Outline each blood parasite and name the species.
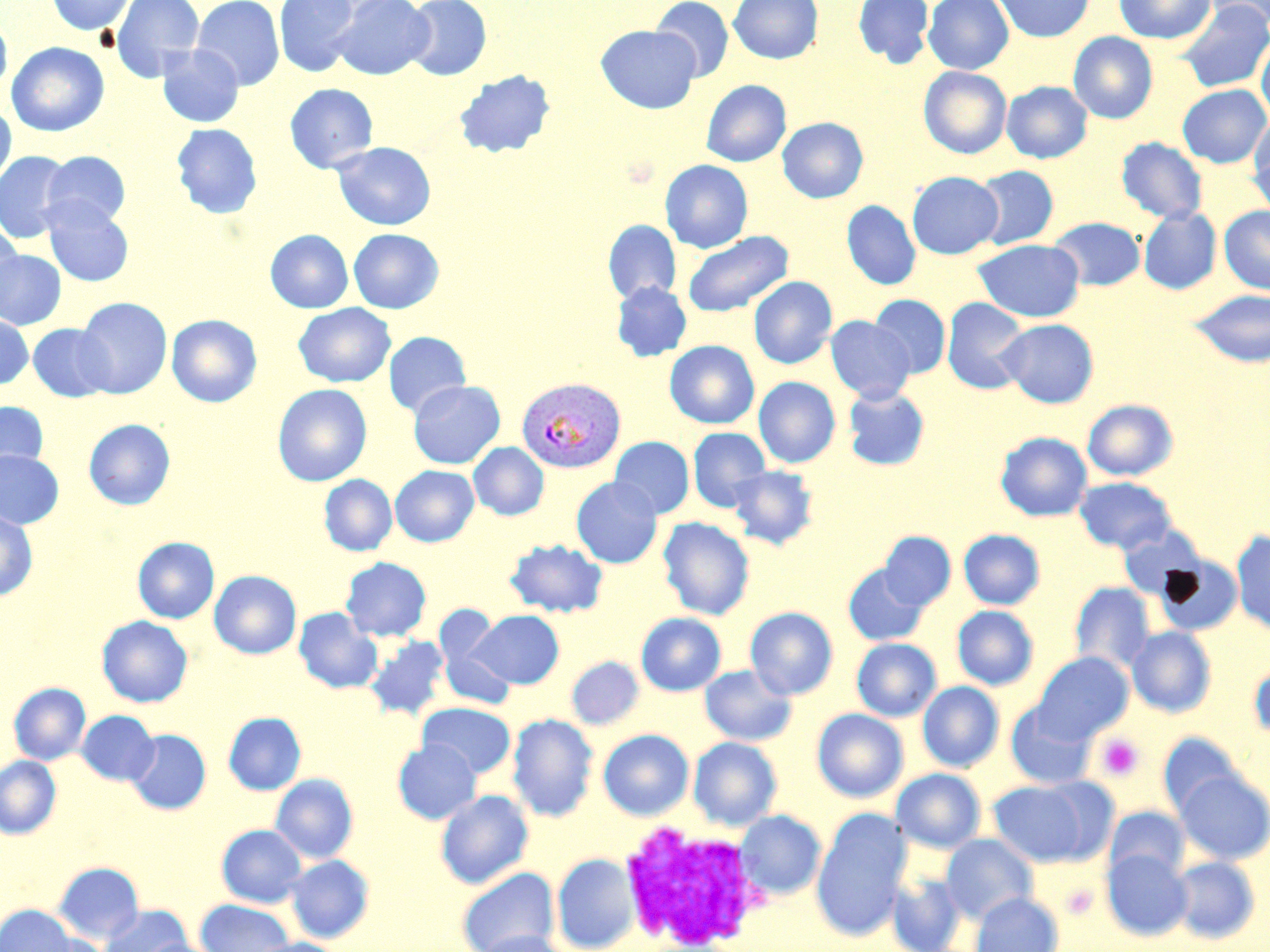

Approximate bounding boxes as (x1,y1)-(x2,y2) corner pairs in pixels.
Plasmodium vivax-infected red blood cells: (517,377)-(625,473).
No Plasmodium falciparum, Plasmodium ovale, Plasmodium malariae, Babesia divergens, or Trypanosoma brucei observed.

slide-level diagnosis = Plasmodium vivax
modality = optical microscopy
magnification = 1000x
preparation = thin blood film
uninfected red blood cell locations = approximate bounding boxes as (x1,y1)-(x2,y2) corner pairs in pixels: (46,0)-(135,35), (110,0)-(204,82), (192,0)-(285,90), (274,0)-(361,77), (330,0)-(434,80), (403,0)-(491,81), (651,0)-(734,82), (729,0)-(823,64), (853,0)-(934,67), (923,0)-(1013,74), (994,0)-(1094,42), (1114,0)-(1216,44), (1203,0)-(1270,30), (1176,1)-(1270,93), (0,15)-(12,99), (596,25)-(700,113), (1068,32)-(1158,123), (1256,32)-(1270,123), (6,42)-(109,137), (156,45)-(244,128), (919,66)-(1011,159), (454,69)-(556,158), (701,80)-(791,167), (1002,81)-(1093,163), (285,83)-(378,173), (1178,84)-(1269,168), (0,103)-(16,190), (1250,115)-(1270,199), (777,117)-(868,203), (171,123)-(262,219), (1117,137)-(1208,224), (331,141)-(436,231), (0,151)-(74,242), (41,151)-(131,230), (660,159)-(753,253), (972,165)-(1059,250), (907,171)-(1003,259), (42,200)-(133,286), (842,200)-(921,290), (1220,206)-(1270,294), (1138,208)-(1221,294), (1049,217)-(1145,290), (603,220)-(681,304), (0,221)-(23,314), (348,228)-(444,313), (265,230)-(353,313), (682,230)-(793,317), (973,239)-(1085,322), (0,249)-(66,330), (748,276)-(837,368), (611,281)-(691,362), (1188,289)-(1270,367), (870,294)-(951,378), (75,297)-(172,398), (942,297)-(1031,394), (293,303)-(395,387), (167,314)-(262,407), (0,315)-(34,388), (826,316)-(915,402), (997,318)-(1099,408), (27,323)-(116,403), (383,331)-(471,417), (664,340)-(759,429), (678,340)-(764,514), (754,376)-(840,468), (408,380)-(505,469), (272,384)-(372,486), (843,385)-(930,470), (1082,399)-(1178,481), (0,401)-(49,476), (83,418)-(176,510), (688,427)-(770,512), (996,432)-(1092,521), (610,436)-(694,519), (468,442)-(548,520), (0,450)-(64,529), (390,465)-(479,547), (728,465)-(818,549), (319,474)-(397,556), (571,476)-(662,568), (1075,476)-(1177,554), (0,509)-(37,601), (658,516)-(755,620), (1117,525)-(1209,602), (958,529)-(1045,609), (1231,530)-(1270,633), (878,532)-(955,611), (133,537)-(219,623), (505,538)-(608,617), (341,557)-(432,641), (843,563)-(930,646), (209,570)-(301,659), (1069,582)-(1156,673), (952,605)-(1038,690), (293,607)-(383,693), (745,607)-(838,699), (469,610)-(564,689), (435,612)-(516,711), (636,613)-(726,696), (97,615)-(193,707), (1126,627)-(1216,717), (364,635)-(451,721), (852,638)-(941,721), (1033,651)-(1133,742), (567,656)-(644,730), (1249,660)-(1270,742), (700,665)-(796,746), (918,681)-(1004,771), (9,682)-(91,765), (417,702)-(516,778), (1006,702)-(1097,789), (812,708)-(908,802), (77,710)-(160,785), (223,712)-(306,795), (507,713)-(598,822), (126,729)-(210,815), (598,729)-(694,820), (1158,732)-(1243,819), (688,737)-(782,830), (392,738)-(481,824), (0,756)-(61,839), (891,768)-(986,853), (1175,769)-(1270,864), (270,773)-(359,863), (988,779)-(1099,867), (435,789)-(534,889), (1105,806)-(1189,883), (812,809)-(912,939), (736,810)-(825,899), (216,824)-(307,907), (941,834)-(1038,922), (1102,848)-(1191,940), (553,852)-(640,952), (285,854)-(374,943), (1171,856)-(1259,944), (52,861)-(145,944), (457,868)-(559,951), (887,871)-(967,952), (970,893)-(1063,952), (194,899)-(295,952), (0,904)-(76,952), (99,904)-(192,952), (473,930)-(575,952), (134,938)-(228,952), (248,938)-(347,952)
stain = May-Grünwald-Giemsa
platelet locations = approximate bounding boxes as (x1,y1)-(x2,y2) corner pairs in pixels: (1096,733)-(1145,782), (1060,883)-(1098,919)
white blood cell locations = approximate bounding boxes as (x1,y1)-(x2,y2) corner pairs in pixels: (618,820)-(767,948)
image size = 1270×952 pixels
field of view = single